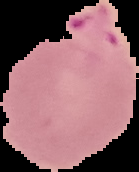
{
  "image_size": "139×172 pixels",
  "preparation": "thin blood film",
  "result": "malaria parasites detected",
  "image_type": "segmented cell region on a black background"
}